Give the extent of all Plasmodium malariae-infected red blood cells.
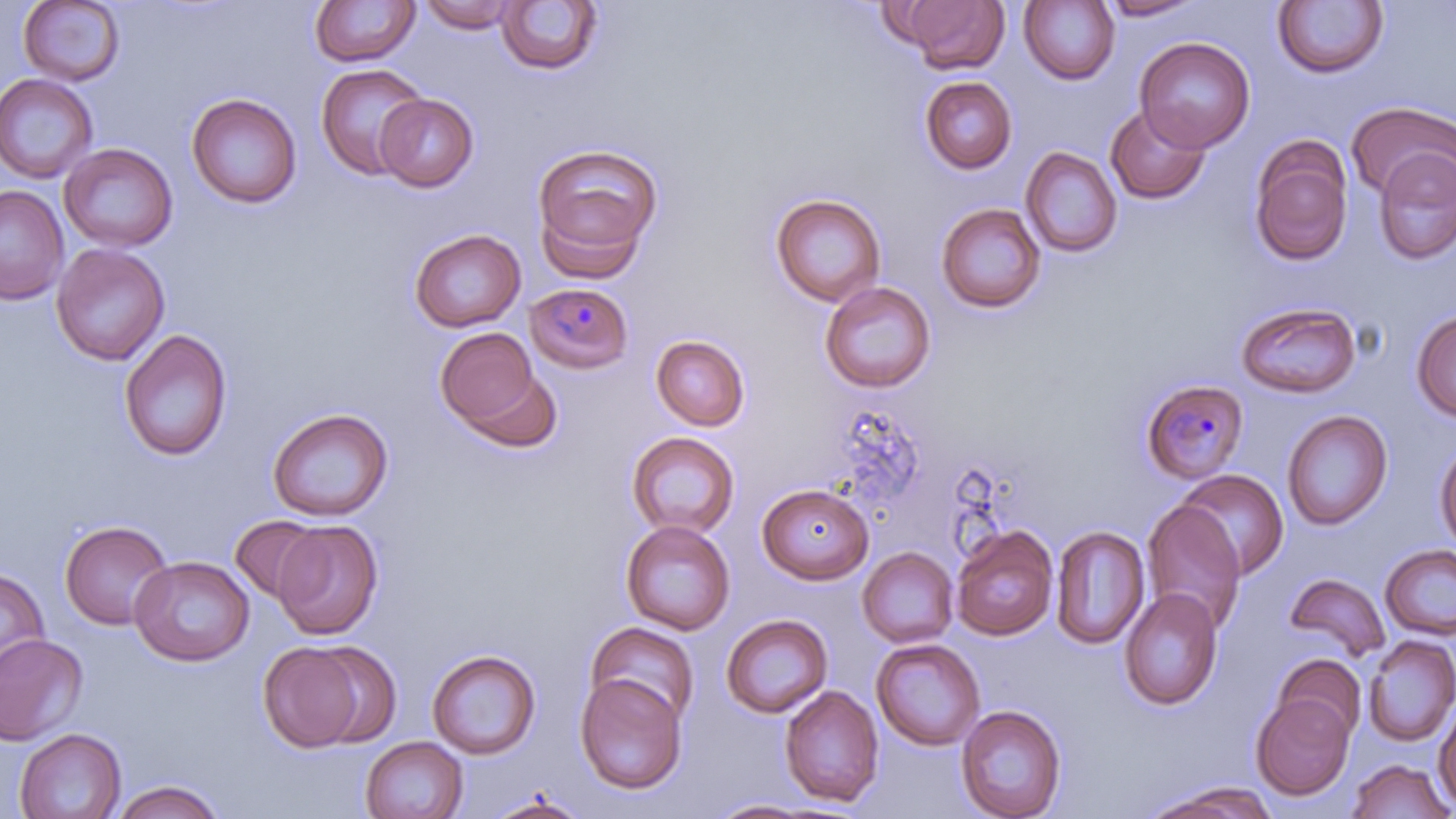

Approximate bounding boxes as named x1/y1/x2/y2 corners in pixels.
Plasmodium malariae-infected red blood cells: (x1=525, y1=282, x2=635, y2=374), (x1=1139, y1=378, x2=1249, y2=485).

Uninfected red blood cell locations: (x1=17, y1=0, x2=126, y2=86), (x1=897, y1=0, x2=1008, y2=74), (x1=1096, y1=0, x2=1206, y2=21), (x1=309, y1=1, x2=420, y2=67), (x1=418, y1=1, x2=522, y2=32), (x1=496, y1=1, x2=603, y2=76), (x1=1019, y1=1, x2=1120, y2=85), (x1=1272, y1=1, x2=1389, y2=79), (x1=1135, y1=37, x2=1255, y2=153), (x1=314, y1=63, x2=428, y2=181), (x1=0, y1=73, x2=99, y2=184), (x1=919, y1=76, x2=1018, y2=174), (x1=186, y1=93, x2=302, y2=209), (x1=374, y1=93, x2=479, y2=192), (x1=1346, y1=100, x2=1456, y2=202), (x1=1105, y1=104, x2=1211, y2=204), (x1=1248, y1=137, x2=1354, y2=267), (x1=531, y1=141, x2=664, y2=275), (x1=59, y1=143, x2=178, y2=252), (x1=1021, y1=146, x2=1122, y2=258), (x1=1373, y1=147, x2=1456, y2=265), (x1=0, y1=185, x2=69, y2=304), (x1=770, y1=193, x2=887, y2=307), (x1=936, y1=202, x2=1046, y2=314), (x1=409, y1=228, x2=526, y2=332), (x1=51, y1=243, x2=170, y2=365), (x1=819, y1=280, x2=937, y2=393), (x1=1235, y1=301, x2=1362, y2=399), (x1=1410, y1=309, x2=1456, y2=423), (x1=434, y1=327, x2=547, y2=437), (x1=119, y1=328, x2=233, y2=461), (x1=650, y1=334, x2=751, y2=431), (x1=267, y1=407, x2=393, y2=522), (x1=1282, y1=409, x2=1393, y2=531), (x1=625, y1=431, x2=740, y2=539), (x1=1434, y1=437, x2=1456, y2=556), (x1=1176, y1=469, x2=1289, y2=580), (x1=757, y1=482, x2=874, y2=584), (x1=1141, y1=500, x2=1247, y2=635), (x1=229, y1=514, x2=328, y2=605), (x1=59, y1=519, x2=173, y2=630), (x1=620, y1=519, x2=736, y2=635), (x1=272, y1=520, x2=383, y2=639), (x1=1051, y1=525, x2=1150, y2=650), (x1=951, y1=526, x2=1058, y2=641), (x1=1380, y1=543, x2=1456, y2=640), (x1=857, y1=546, x2=959, y2=648), (x1=129, y1=555, x2=254, y2=666), (x1=0, y1=568, x2=50, y2=680), (x1=1284, y1=572, x2=1390, y2=663), (x1=1119, y1=588, x2=1223, y2=711), (x1=720, y1=614, x2=834, y2=718), (x1=585, y1=622, x2=700, y2=725), (x1=0, y1=634, x2=88, y2=746), (x1=1362, y1=635, x2=1456, y2=747), (x1=871, y1=638, x2=986, y2=751), (x1=258, y1=642, x2=366, y2=752), (x1=309, y1=643, x2=402, y2=748), (x1=427, y1=649, x2=541, y2=759), (x1=1272, y1=653, x2=1366, y2=743), (x1=574, y1=672, x2=688, y2=795), (x1=779, y1=685, x2=884, y2=807), (x1=1251, y1=692, x2=1355, y2=800), (x1=1433, y1=698, x2=1456, y2=811), (x1=955, y1=704, x2=1067, y2=819), (x1=14, y1=728, x2=126, y2=818), (x1=360, y1=736, x2=469, y2=819), (x1=1347, y1=758, x2=1454, y2=819), (x1=110, y1=780, x2=225, y2=819), (x1=1145, y1=783, x2=1279, y2=818), (x1=482, y1=792, x2=591, y2=818), (x1=708, y1=798, x2=824, y2=817). Slide-level diagnosis: Plasmodium malariae. Thin blood film. May-Grünwald-Giemsa-stained preparation. 1000x magnification. Optical microscopy. Image is 1456×819 pixels. One field of a larger specimen.